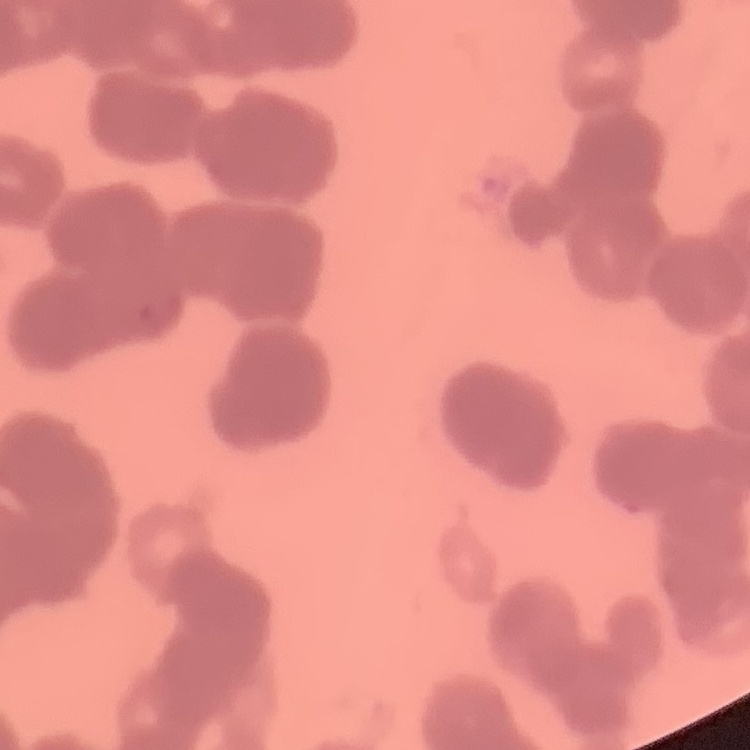

Summary:
  - Red blood cell morphology: rouleaux formation
  - Preparation: thin peripheral smear
  - Image type: one tile cut from a larger photomicrograph
  - Stain: Field's or Giemsa